State which parasite is depicted.
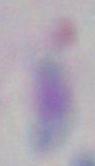

This is Toxoplasma gondii.

Micrograph. Captured at 1000x magnification.